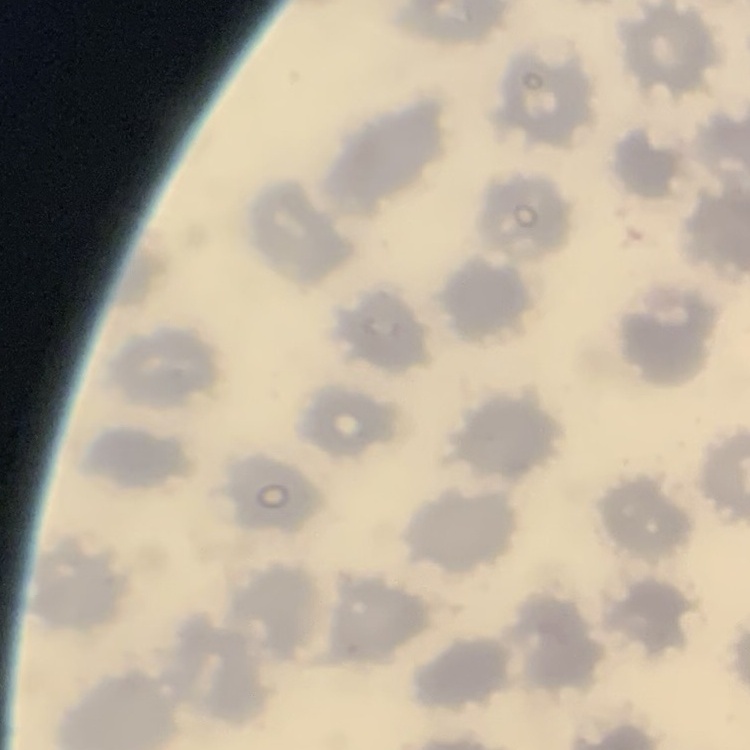
The red blood cells show no rouleaux formation. One tile cut from a larger photomicrograph. Thin blood film. Stained with either Field's or Giemsa.